Identify the cell.
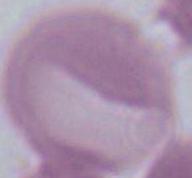

An erythrocyte.

1000x magnification. Micrograph.